Locate every blood parasite and identify its species.
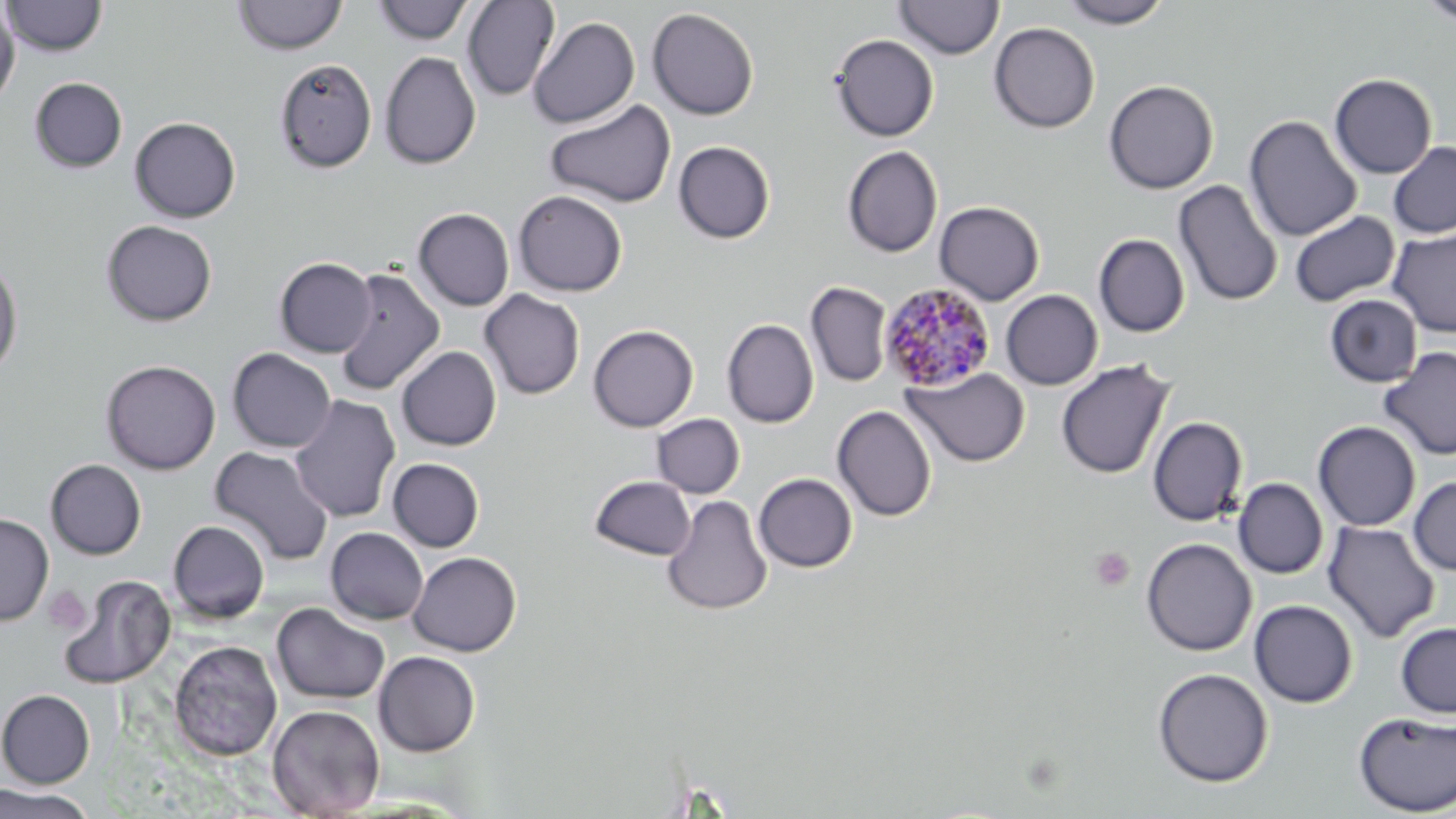

Approximate bounding boxes as named x1/y1/x2/y2 corners in pixels.
Plasmodium malariae-infected red blood cells: (x1=878, y1=281, x2=996, y2=392).
No Plasmodium falciparum, Plasmodium ovale, Plasmodium vivax, Babesia divergens, or Trypanosoma brucei observed.

Uninfected red blood cell locations: (x1=2, y1=0, x2=108, y2=57), (x1=1057, y1=0, x2=1173, y2=28), (x1=1417, y1=0, x2=1456, y2=26), (x1=232, y1=1, x2=348, y2=55), (x1=373, y1=1, x2=474, y2=45), (x1=462, y1=1, x2=560, y2=100), (x1=894, y1=1, x2=1004, y2=59), (x1=0, y1=5, x2=20, y2=107), (x1=647, y1=7, x2=759, y2=120), (x1=528, y1=16, x2=640, y2=128), (x1=989, y1=22, x2=1100, y2=133), (x1=830, y1=34, x2=939, y2=141), (x1=379, y1=51, x2=481, y2=170), (x1=274, y1=57, x2=378, y2=173), (x1=1329, y1=74, x2=1437, y2=178), (x1=29, y1=77, x2=127, y2=173), (x1=1103, y1=80, x2=1218, y2=194), (x1=544, y1=99, x2=676, y2=208), (x1=1244, y1=115, x2=1362, y2=242), (x1=130, y1=116, x2=241, y2=223), (x1=673, y1=141, x2=775, y2=244), (x1=1388, y1=142, x2=1456, y2=238), (x1=842, y1=146, x2=942, y2=258), (x1=1173, y1=179, x2=1283, y2=307), (x1=513, y1=190, x2=628, y2=296), (x1=934, y1=201, x2=1044, y2=305), (x1=413, y1=208, x2=514, y2=311), (x1=1290, y1=210, x2=1400, y2=306), (x1=101, y1=220, x2=217, y2=326), (x1=1388, y1=228, x2=1456, y2=337), (x1=1093, y1=234, x2=1190, y2=337), (x1=0, y1=256, x2=24, y2=379), (x1=275, y1=257, x2=377, y2=358), (x1=332, y1=267, x2=444, y2=396), (x1=805, y1=282, x2=892, y2=387), (x1=480, y1=289, x2=585, y2=400), (x1=1000, y1=290, x2=1102, y2=390), (x1=1324, y1=294, x2=1422, y2=387), (x1=722, y1=319, x2=819, y2=428), (x1=587, y1=325, x2=698, y2=432), (x1=396, y1=346, x2=501, y2=451), (x1=1378, y1=346, x2=1456, y2=461), (x1=227, y1=348, x2=336, y2=452), (x1=100, y1=359, x2=221, y2=475), (x1=1057, y1=359, x2=1174, y2=480), (x1=902, y1=367, x2=1030, y2=467), (x1=288, y1=394, x2=401, y2=523), (x1=832, y1=405, x2=936, y2=522), (x1=652, y1=413, x2=745, y2=498), (x1=1148, y1=416, x2=1248, y2=526), (x1=1313, y1=421, x2=1421, y2=531), (x1=209, y1=445, x2=334, y2=565), (x1=388, y1=458, x2=484, y2=552), (x1=45, y1=459, x2=146, y2=560), (x1=754, y1=473, x2=857, y2=573), (x1=589, y1=476, x2=696, y2=560), (x1=1408, y1=476, x2=1456, y2=576), (x1=1233, y1=479, x2=1328, y2=579), (x1=662, y1=494, x2=772, y2=616), (x1=0, y1=514, x2=54, y2=625), (x1=168, y1=520, x2=270, y2=623), (x1=1323, y1=521, x2=1440, y2=643), (x1=325, y1=527, x2=428, y2=625), (x1=1141, y1=537, x2=1257, y2=656), (x1=408, y1=551, x2=521, y2=656), (x1=59, y1=574, x2=175, y2=689), (x1=1249, y1=600, x2=1358, y2=707), (x1=271, y1=602, x2=390, y2=705), (x1=1396, y1=621, x2=1456, y2=718), (x1=168, y1=640, x2=283, y2=761), (x1=373, y1=651, x2=480, y2=756), (x1=1152, y1=667, x2=1273, y2=788), (x1=0, y1=689, x2=96, y2=789), (x1=267, y1=704, x2=384, y2=818), (x1=1353, y1=711, x2=1456, y2=816), (x1=0, y1=783, x2=98, y2=819). Platelet locations: (x1=1090, y1=547, x2=1134, y2=591), (x1=44, y1=585, x2=91, y2=634). Slide-level diagnosis: Plasmodium malariae. One field of a larger specimen. May-Grünwald-Giemsa stain. 1000x magnification. Optical microscopy. Image is 1456×819 pixels. Thin blood smear.